Give the extent of all Plasmodium falciparum-infected red blood cells.
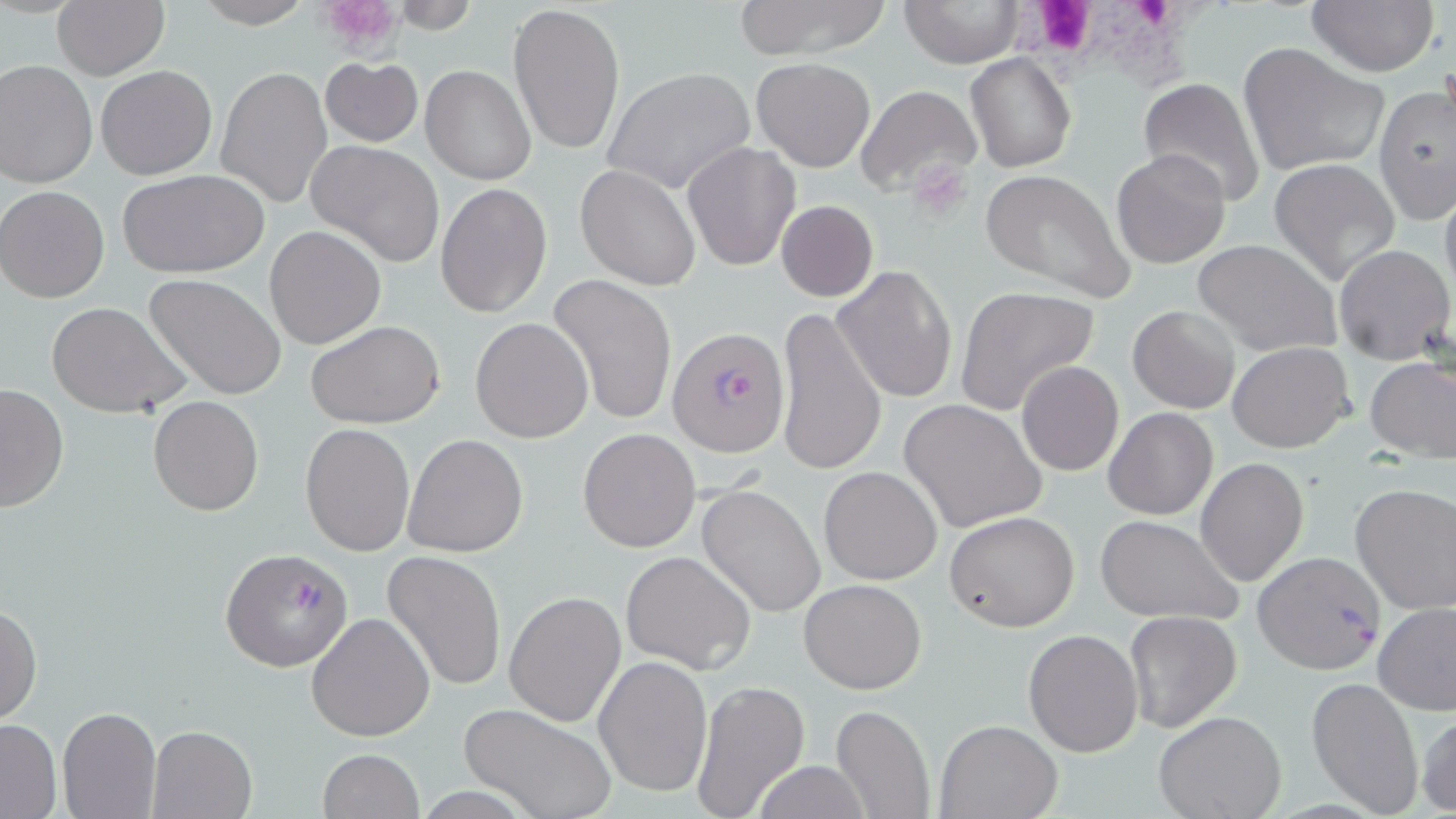
Approximate bounding boxes as [x1, y1, x2, y2] in pixels.
Plasmodium falciparum-infected red blood cells: [668, 326, 791, 456], [222, 547, 352, 671], [1252, 552, 1388, 673].

{
  "slide_level_diagnosis": "Plasmodium falciparum",
  "platelet_locations": "approximate bounding boxes as [x1, y1, x2, y2] in pixels: [319, 0, 405, 52], [911, 161, 975, 220]",
  "stain": "May-Grünwald-Giemsa",
  "preparation": "thin blood film",
  "modality": "light microscopy",
  "magnification": "1000x",
  "white_blood_cell_locations": "approximate bounding boxes as [x1, y1, x2, y2] in pixels: [1019, 2, 1231, 87]",
  "uninfected_red_blood_cell_locations": "approximate bounding boxes as [x1, y1, x2, y2] in pixels: [51, 0, 169, 80], [192, 0, 313, 28], [733, 0, 892, 59], [898, 0, 1023, 67], [1304, 0, 1439, 75], [507, 2, 625, 155], [1238, 41, 1392, 177], [966, 51, 1077, 173], [320, 57, 423, 147], [752, 58, 874, 172], [0, 60, 97, 187], [421, 64, 538, 185], [95, 65, 218, 180], [216, 67, 331, 208], [602, 67, 756, 196], [1137, 78, 1266, 210], [857, 85, 982, 199], [1375, 85, 1455, 223], [306, 140, 445, 268], [683, 141, 800, 271], [1111, 149, 1232, 267], [1270, 158, 1401, 287], [575, 164, 701, 291], [976, 167, 1136, 306], [117, 169, 270, 277], [1439, 181, 1456, 307], [436, 183, 553, 319], [0, 185, 110, 304], [775, 199, 876, 302], [264, 224, 387, 350], [1192, 238, 1341, 357], [1333, 243, 1453, 365], [832, 265, 958, 404], [143, 273, 289, 400], [547, 273, 679, 424], [953, 286, 1100, 417], [46, 302, 190, 418], [1128, 304, 1241, 414], [775, 305, 887, 477], [470, 317, 594, 442], [304, 319, 446, 428], [1229, 342, 1354, 452], [1364, 357, 1456, 460], [1015, 361, 1124, 476], [0, 382, 70, 513], [147, 395, 264, 516], [899, 400, 1046, 533], [1103, 407, 1217, 520], [301, 424, 415, 556], [578, 427, 702, 551], [403, 433, 529, 558], [1196, 457, 1308, 585], [818, 465, 943, 585], [696, 482, 827, 619], [1351, 483, 1456, 614], [944, 510, 1081, 631], [1093, 513, 1243, 625], [383, 551, 508, 692], [621, 551, 756, 675], [798, 578, 927, 694], [504, 590, 627, 727], [1373, 602, 1455, 715], [0, 603, 43, 726], [1124, 609, 1243, 733], [306, 612, 436, 742], [1023, 628, 1144, 756], [592, 655, 712, 799], [1305, 676, 1426, 817], [691, 681, 811, 819], [830, 702, 936, 819], [459, 703, 616, 819], [58, 707, 162, 819], [1415, 708, 1456, 816], [1154, 711, 1286, 819], [0, 718, 62, 817], [936, 719, 1060, 818], [146, 725, 257, 819], [317, 749, 425, 819], [753, 760, 874, 819]",
  "field_of_view": "one of a larger specimen",
  "image_size": "1456×819 pixels"
}